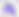

Captured at 400x magnification. Micrograph. Toxoplasma gondii is shown.